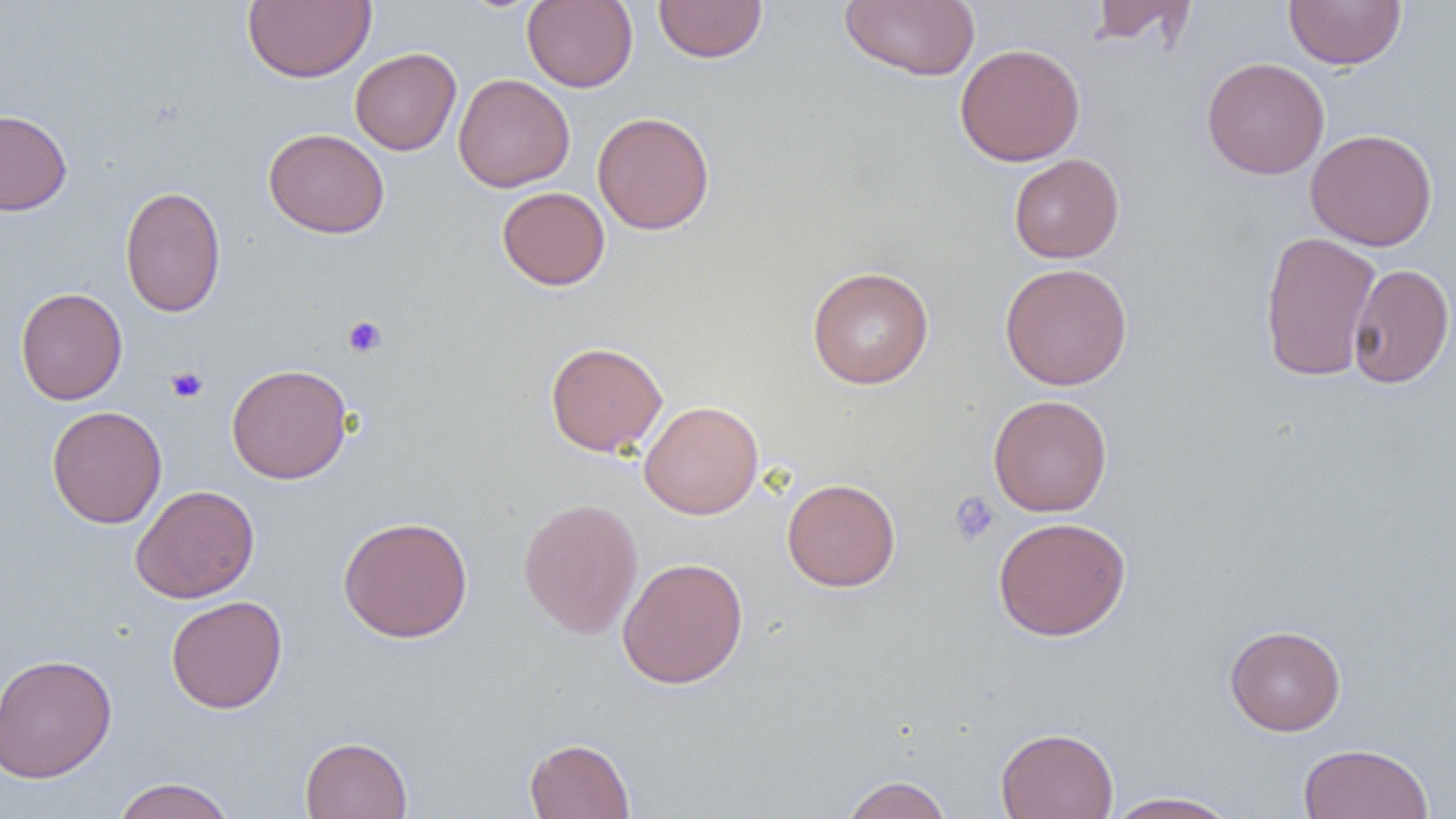
slide-level diagnosis = no evidence of blood parasites
modality = light microscopy
uninfected red blood cell locations = approximate bounding boxes as (x1,y1)-(x2,y2) corner pairs in pixels: (242,0)-(376,83), (653,0)-(767,63), (1087,0)-(1197,48), (1284,0)-(1406,69), (522,1)-(638,92), (839,1)-(981,80), (955,43)-(1086,166), (350,47)-(461,155), (1201,57)-(1329,180), (453,73)-(574,192), (0,108)-(72,216), (593,111)-(715,235), (263,128)-(389,239), (1306,129)-(1438,251), (1009,153)-(1125,263), (119,185)-(227,318), (497,186)-(610,290), (1258,231)-(1382,382), (999,262)-(1133,390), (1348,263)-(1455,389), (806,266)-(934,390), (15,287)-(127,405), (544,341)-(668,457), (226,363)-(353,484), (987,395)-(1113,517), (639,400)-(764,519), (46,405)-(167,528), (782,478)-(900,592), (130,484)-(260,604), (518,497)-(643,639), (338,515)-(473,643), (993,516)-(1131,641), (617,556)-(748,689), (166,595)-(288,714), (1224,624)-(1346,736), (0,653)-(117,783), (995,726)-(1119,819), (299,736)-(413,819), (524,737)-(635,818), (1297,743)-(1434,818), (840,775)-(951,819), (111,777)-(237,819), (1103,790)-(1241,819)
platelet locations = approximate bounding boxes as (x1,y1)-(x2,y2) corner pairs in pixels: (343,316)-(387,358), (166,366)-(208,403), (948,491)-(1000,546)
field of view = single
image size = 1456×819 pixels
preparation = thin blood film
magnification = 1000x